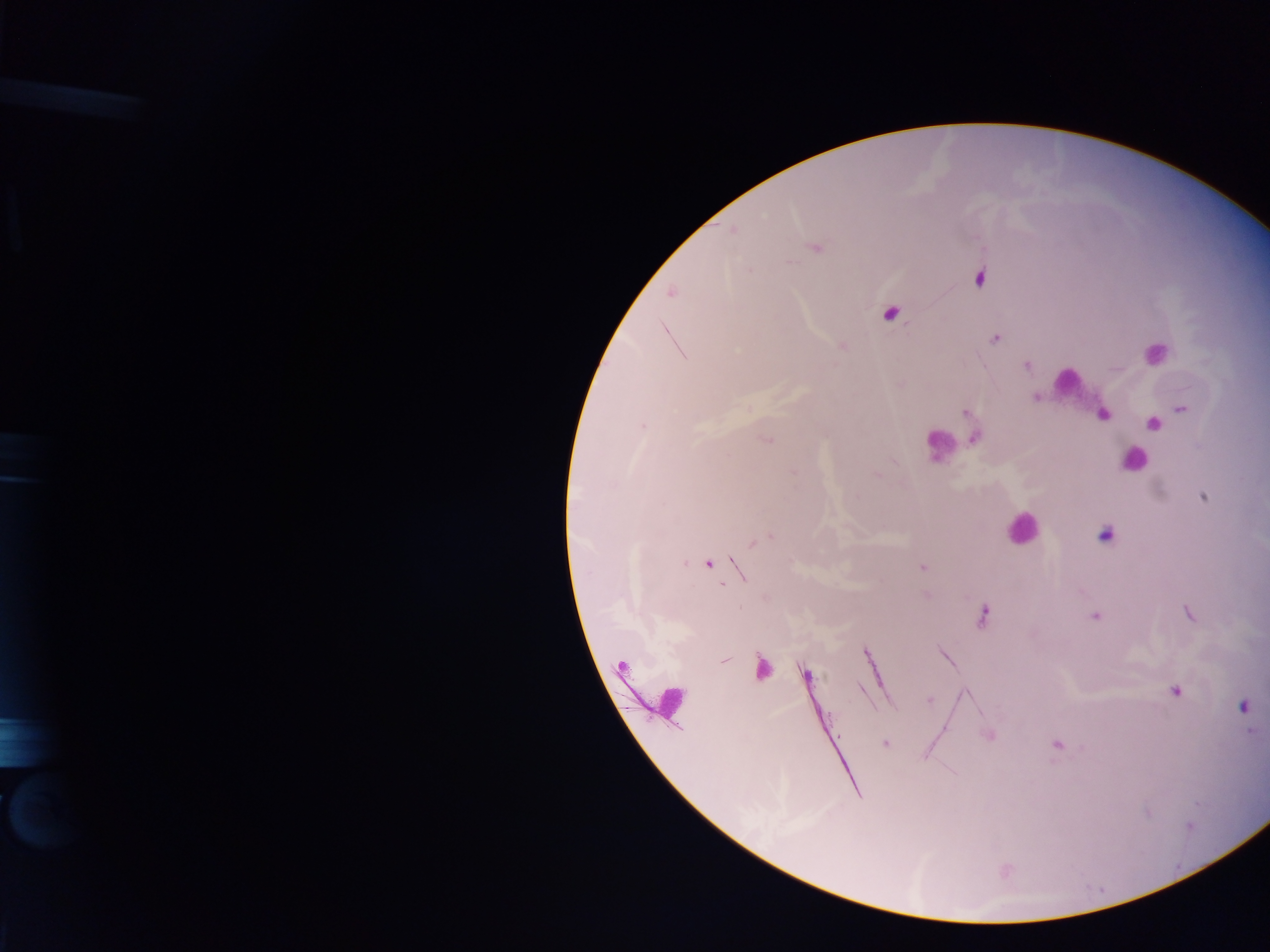

Approximate centers as {x, y} in pixels. Malaria parasite locations: {732, 231}, {816, 247}, {790, 262}, {980, 277}, {670, 293}, {890, 313}, {996, 339}, {1026, 365}, {1036, 397}, {1182, 409}, {966, 413}, {1103, 414}, {1153, 424}, {643, 426}, {974, 439}, {766, 440}, {877, 476}, {1203, 496}, {1105, 535}, {759, 541}, {685, 563}, {709, 564}, {923, 567}, {742, 571}, {927, 595}, {1188, 614}, {982, 615}, {1095, 616}, {945, 656}, {725, 659}, {761, 668}, {806, 674}, {1176, 691}, {929, 699}, {1244, 706}, {989, 735}, {885, 744}, {1057, 745}. Leukocyte locations: {1154, 353}, {1067, 382}, {939, 445}, {1133, 461}, {1021, 527}, {670, 700}. Mobile-phone photograph taken through the microscope. Thick blood smear. Collected in Ghana. Image is 1270×952 pixels. Single field of view.